Assess this cell for malaria.
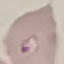
Parasitized.

Summary:
  - Preparation: thin smear
  - Image type: cell patch, automatically extracted from a larger field of view and resized to 64 × 64 pixels
  - Capture: smartphone through the microscope eyepiece
  - Stain: Giemsa